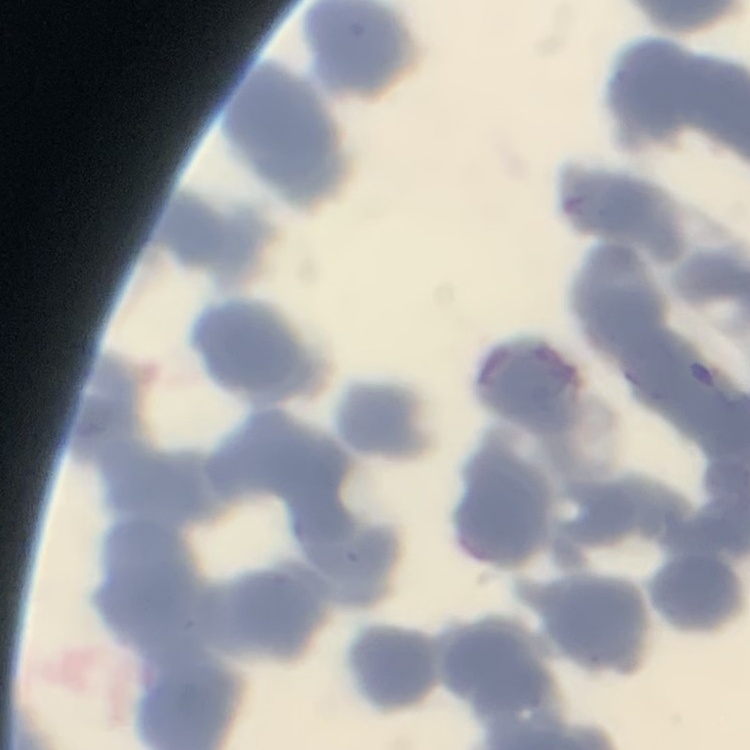
Summary:
  - Red blood cell morphology: rouleaux formation
  - Image type: one tile cut from a larger photomicrograph
  - Stain: Field's or Giemsa
  - Preparation: thin blood film